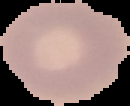
{
  "malaria_status": "uninfected",
  "preparation": "thin blood film",
  "image_type": "segmented cell region on a black background",
  "image_size": "130×106 pixels"
}